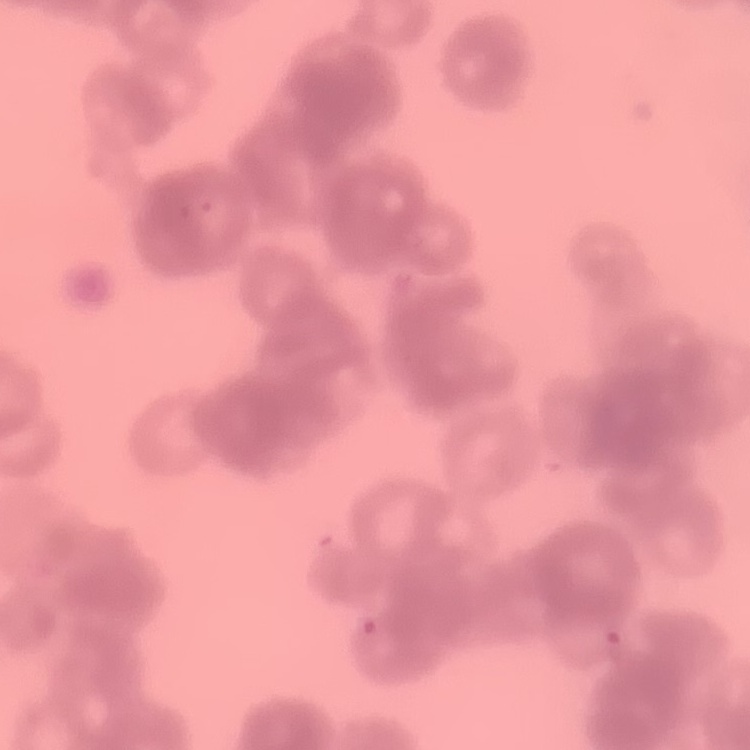 The red blood cells show rouleaux formation. One tile cut from a larger photomicrograph. Field's or Giemsa stain. Thin blood smear.